Identify the blood parasite species.
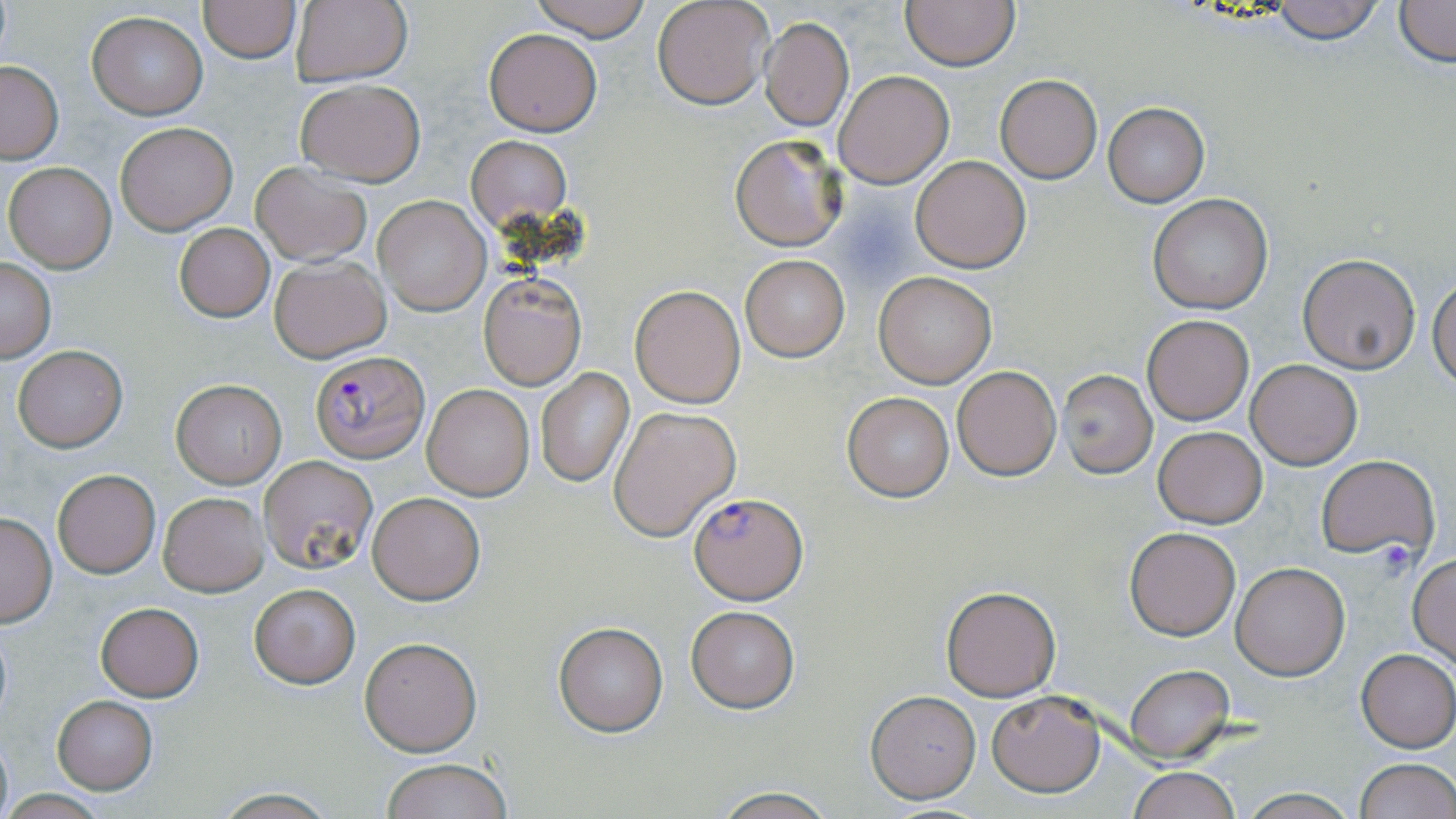

Plasmodium falciparum.

modality = light microscopy
stain = May-Grünwald-Giemsa
preparation = thin blood film
image size = 1456×819 pixels
Plasmodium falciparum-infected red blood cell locations = approximate bounding boxes as [x1, y1, x2, y2] in pixels: [309, 349, 428, 461], [687, 491, 806, 602]
magnification = 1000x
field of view = single
uninfected red blood cell locations = approximate bounding boxes as [x1, y1, x2, y2] in pixels: [528, 0, 655, 42], [650, 0, 773, 110], [901, 0, 1019, 71], [1267, 0, 1387, 44], [1390, 0, 1454, 68], [198, 1, 301, 63], [290, 2, 413, 85], [87, 11, 207, 118], [761, 17, 853, 129], [483, 28, 602, 136], [0, 60, 62, 161], [832, 70, 954, 188], [994, 73, 1103, 184], [294, 78, 426, 185], [1103, 103, 1210, 207], [115, 120, 238, 235], [730, 133, 847, 250], [465, 135, 571, 230], [912, 155, 1031, 272], [4, 161, 117, 272], [250, 162, 373, 267], [1147, 194, 1272, 314], [374, 196, 490, 315], [173, 222, 275, 322], [1297, 254, 1420, 373], [269, 255, 391, 362], [740, 255, 850, 361], [1, 258, 56, 361], [874, 272, 997, 388], [479, 275, 586, 390], [1429, 276, 1455, 390], [629, 283, 746, 408], [1140, 314, 1255, 425], [11, 344, 128, 452], [1246, 357, 1362, 470], [952, 365, 1061, 480], [536, 368, 633, 488], [1058, 368, 1158, 477], [169, 378, 286, 488], [423, 384, 534, 500], [843, 391, 954, 502], [609, 405, 741, 542], [1153, 426, 1268, 528], [1316, 455, 1438, 562], [259, 456, 376, 573], [52, 467, 161, 579], [159, 492, 269, 596], [367, 492, 485, 604], [0, 512, 58, 626], [1124, 528, 1241, 640], [1408, 555, 1455, 665], [1230, 563, 1349, 680], [249, 582, 359, 688], [941, 584, 1061, 701], [95, 602, 203, 701], [686, 606, 799, 712], [554, 622, 669, 736], [359, 637, 482, 756], [1356, 649, 1456, 752], [1125, 665, 1234, 761], [865, 688, 981, 804], [987, 689, 1105, 796], [52, 696, 158, 793], [1354, 758, 1455, 819], [380, 759, 513, 818], [1126, 766, 1240, 819], [1237, 788, 1358, 819], [212, 789, 340, 818], [708, 789, 839, 818]